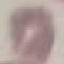 Result: no malaria parasites detected. Giemsa stain. Acquired by smartphone through the microscope eyepiece. Cell patch, automatically extracted from a larger field of view and resized to 64 × 64 pixels. Thin blood film.